Report the malaria status of this cell.
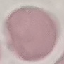

It is uninfected.

Summary:
  - Preparation: thin blood film
  - Capture: smartphone camera at the microscope eyepiece
  - Stain: Giemsa
  - Image type: cell patch, automatically extracted from a larger field of view and resized to 64 × 64 pixels